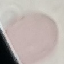
result = no malaria parasites detected
capture = smartphone camera at the microscope eyepiece
stain = Giemsa
image type = automatically extracted cell patch, resized to 64 × 64 pixels
preparation = thin blood smear